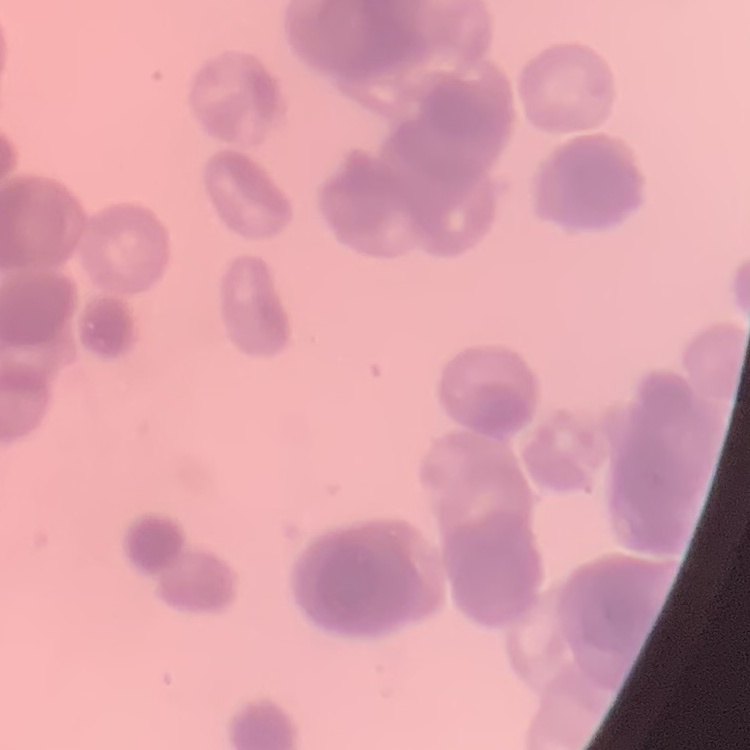
The erythrocytes show rouleaux formation. Field's or Giemsa stain. Thin blood smear. One tile cut from a larger photomicrograph.